Name the parasite shown.
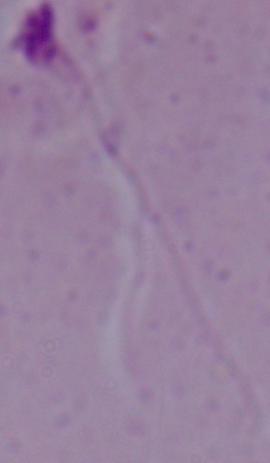
Leishmania.

modality = photomicrograph
magnification = 1000x